Locate and identify every blood parasite.
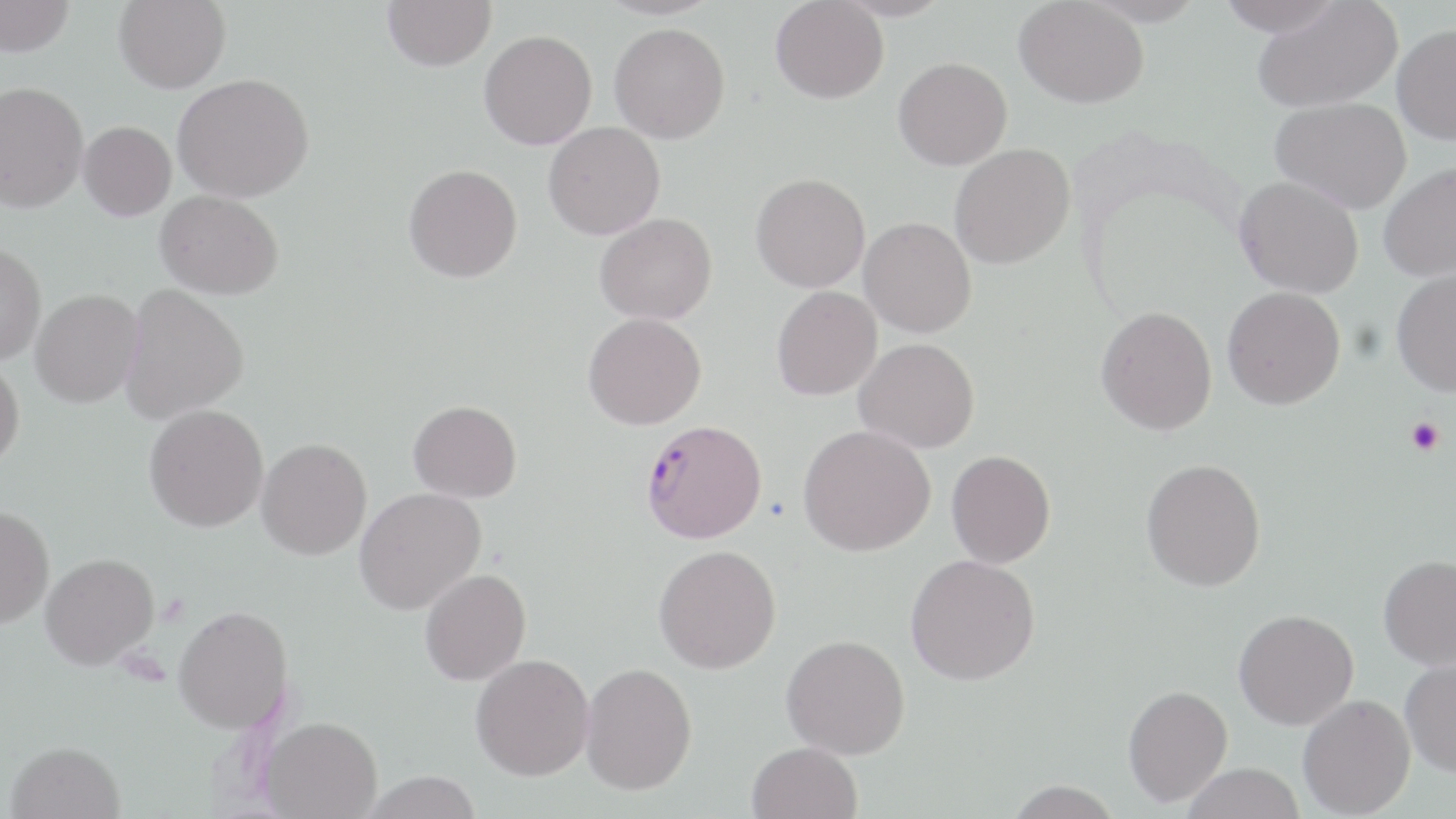

Approximate bounding boxes as (x1, y1, x2, y2) in pixels.
Plasmodium falciparum-infected red blood cells: (639, 420, 768, 544).
No Plasmodium ovale, Plasmodium malariae, Plasmodium vivax, Babesia divergens, or Trypanosoma brucei observed.

Uninfected red blood cell locations: (0, 0, 75, 56), (114, 0, 230, 93), (383, 0, 496, 71), (770, 0, 889, 103), (836, 0, 953, 21), (1014, 0, 1149, 107), (1216, 0, 1343, 37), (1252, 1, 1403, 113), (609, 22, 730, 143), (1392, 24, 1456, 145), (478, 30, 597, 150), (893, 57, 1012, 170), (172, 72, 314, 202), (0, 81, 89, 213), (1270, 97, 1412, 213), (78, 120, 177, 220), (543, 122, 665, 239), (949, 143, 1075, 269), (1378, 162, 1456, 282), (404, 163, 522, 282), (750, 173, 870, 293), (1234, 175, 1364, 297), (155, 190, 284, 299), (594, 213, 717, 325), (859, 217, 977, 338), (0, 242, 47, 365), (1391, 269, 1456, 397), (119, 283, 249, 424), (771, 286, 882, 400), (1222, 286, 1345, 410), (30, 289, 144, 408), (1096, 306, 1217, 435), (583, 312, 706, 430), (854, 338, 980, 453), (0, 358, 24, 473), (408, 400, 522, 502), (144, 404, 269, 532), (797, 424, 935, 556), (256, 438, 372, 559), (946, 450, 1055, 568), (1141, 457, 1266, 591), (354, 487, 486, 615), (0, 506, 54, 628), (653, 545, 781, 673), (41, 553, 159, 669), (905, 553, 1040, 685), (1378, 554, 1456, 670), (420, 568, 531, 685), (173, 605, 293, 733), (1234, 609, 1359, 730), (781, 634, 910, 759), (471, 654, 595, 780), (1400, 657, 1456, 776), (580, 662, 697, 795), (1123, 684, 1232, 807), (1297, 694, 1416, 818), (261, 716, 382, 818), (6, 741, 125, 819), (747, 741, 862, 819), (1180, 763, 1306, 819), (359, 771, 484, 819), (1002, 780, 1125, 818). Platelet locations: (1405, 416, 1444, 456). Slide-level diagnosis: Plasmodium falciparum. Thin blood smear. Single field of view. May-Grünwald-Giemsa stain. 1000x magnification. Image is 1456×819 pixels. Optical microscopy.